State the blood parasite species.
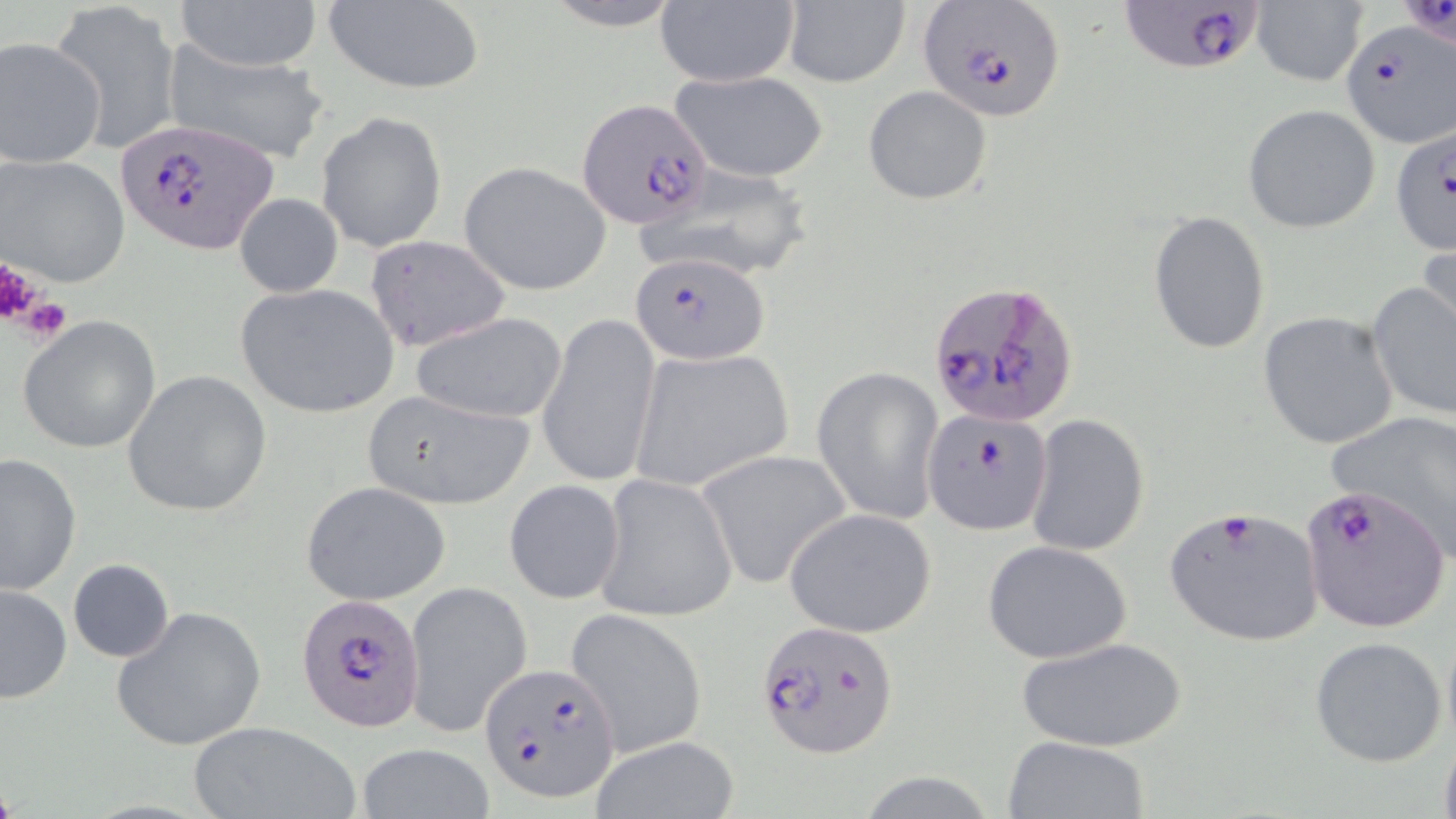
Plasmodium falciparum.

Summary:
  - Coordinate format: approximate bounding boxes as (x1, y1, x2, y2) in pixels
  - Platelet locations: (0, 256, 39, 327), (17, 298, 71, 342)
  - Plasmodium falciparum-infected red blood cell locations: (1120, 0, 1268, 75), (919, 1, 1067, 122), (1341, 19, 1455, 147), (580, 99, 712, 227), (116, 118, 281, 257), (1389, 124, 1456, 254), (631, 251, 771, 364), (930, 281, 1079, 429), (1298, 481, 1451, 632), (294, 590, 426, 731), (755, 618, 898, 757), (480, 664, 619, 804)
  - Uninfected red blood cell locations: (172, 0, 326, 72), (540, 0, 686, 29), (654, 0, 796, 88), (1249, 0, 1368, 87), (319, 1, 486, 96), (782, 1, 911, 88), (51, 2, 182, 154), (0, 35, 107, 169), (162, 39, 331, 166), (669, 69, 830, 183), (863, 85, 993, 205), (1243, 104, 1381, 234), (316, 111, 448, 254), (1, 154, 131, 289), (459, 161, 612, 296), (636, 161, 814, 283), (234, 194, 343, 298), (1147, 210, 1270, 354), (1419, 229, 1456, 353), (367, 235, 509, 357), (1367, 280, 1456, 422), (235, 283, 398, 418), (1258, 310, 1398, 450), (410, 311, 569, 426), (539, 311, 658, 491), (18, 313, 161, 452), (631, 348, 791, 491), (812, 367, 944, 525), (121, 369, 271, 518), (360, 388, 536, 509), (1326, 409, 1456, 556), (920, 410, 1090, 538), (1026, 414, 1150, 557), (0, 452, 81, 596), (700, 452, 853, 593), (594, 473, 739, 623), (505, 480, 625, 604), (301, 481, 452, 606), (1164, 505, 1325, 646), (785, 509, 937, 635), (981, 540, 1134, 664), (67, 559, 175, 663), (404, 578, 531, 740), (0, 584, 72, 704), (111, 604, 267, 751), (565, 609, 708, 759), (1308, 635, 1448, 768), (1014, 637, 1189, 752), (188, 721, 361, 819), (1439, 732, 1456, 819), (590, 735, 740, 819), (1002, 735, 1151, 818), (356, 742, 495, 818)
  - Preparation: thin blood smear
  - Field of view: one of a larger specimen
  - Image size: 1456×819 pixels
  - Modality: optical microscopy
  - Magnification: 1000x
  - Stain: May-Grünwald-Giemsa